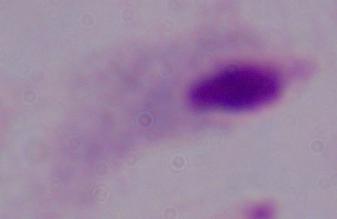

Summary:
  - Identification: trichomonad
  - Modality: photomicrograph
  - Magnification: 1000x